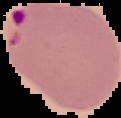
image size = 121×118 pixels
preparation = thin blood film
malaria status = parasitized
image type = segmented cell region on a black background